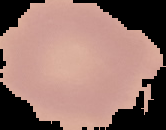
Summary:
  - Preparation: thin blood smear
  - Result: negative for malaria parasites
  - Image type: segmented cell region with the area outside set to black
  - Image size: 166×130 pixels